Report the malaria status of this cell.
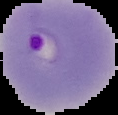

Parasitized.

From a thin blood film. Segmented cell region on a black background. Image is 118×115 pixels.